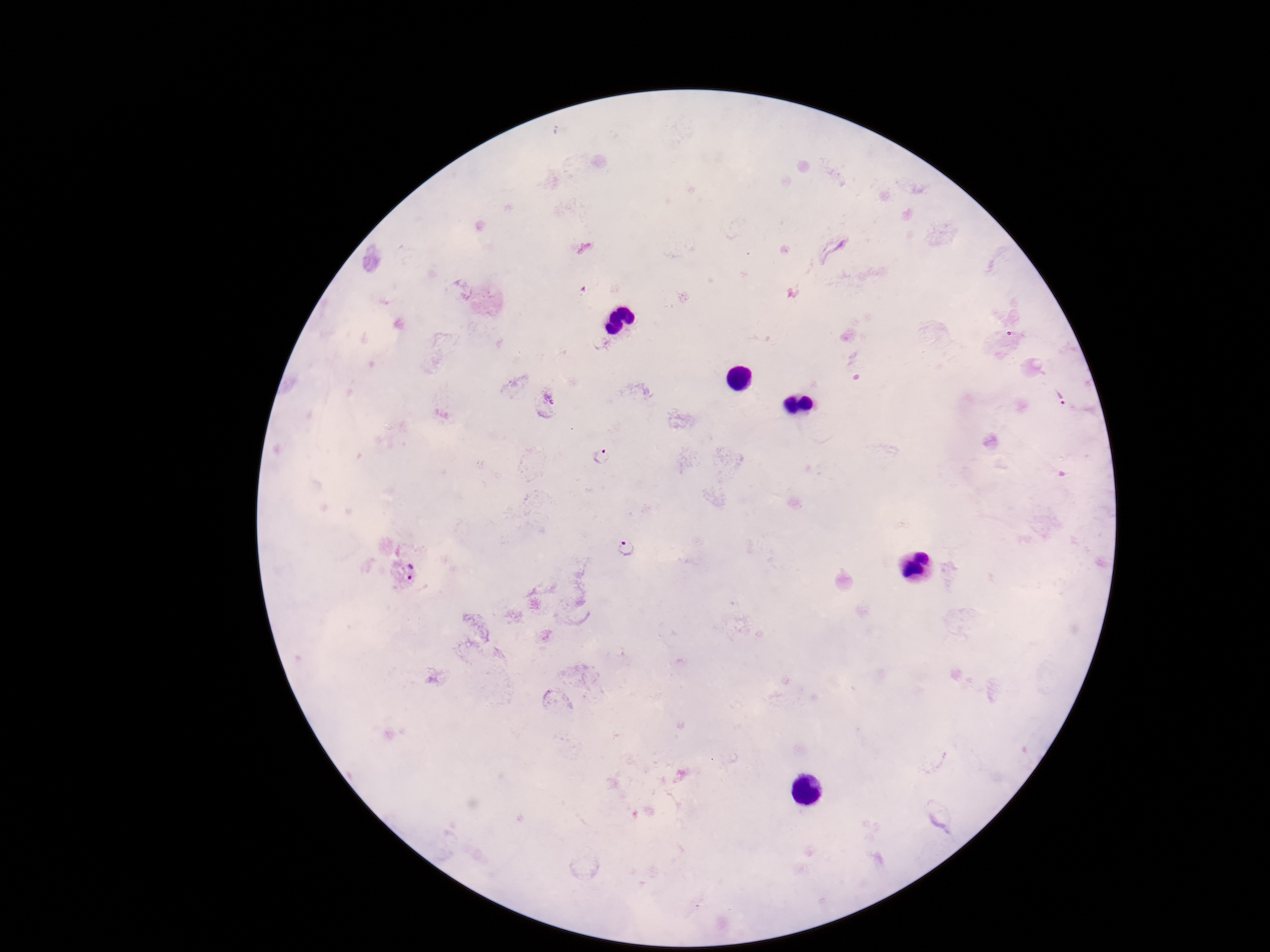

Approximate centers as (x, y) in pixels. Plasmodium parasite locations: (1061, 397), (547, 401), (602, 456), (626, 547), (405, 571). Single field of view. Patient malaria status: positive. 100x magnification. Giemsa-stained preparation. Image is 1270×952 pixels. Smartphone photograph taken through the microscope eyepiece. Thick blood smear.